Report the malaria status of this cell.
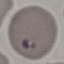

Parasitized.

Summary:
  - Stain: Giemsa
  - Preparation: thin blood film
  - Image type: cell patch, automatically extracted from a larger field of view and resized to 64 × 64 pixels
  - Capture: smartphone camera at the microscope eyepiece